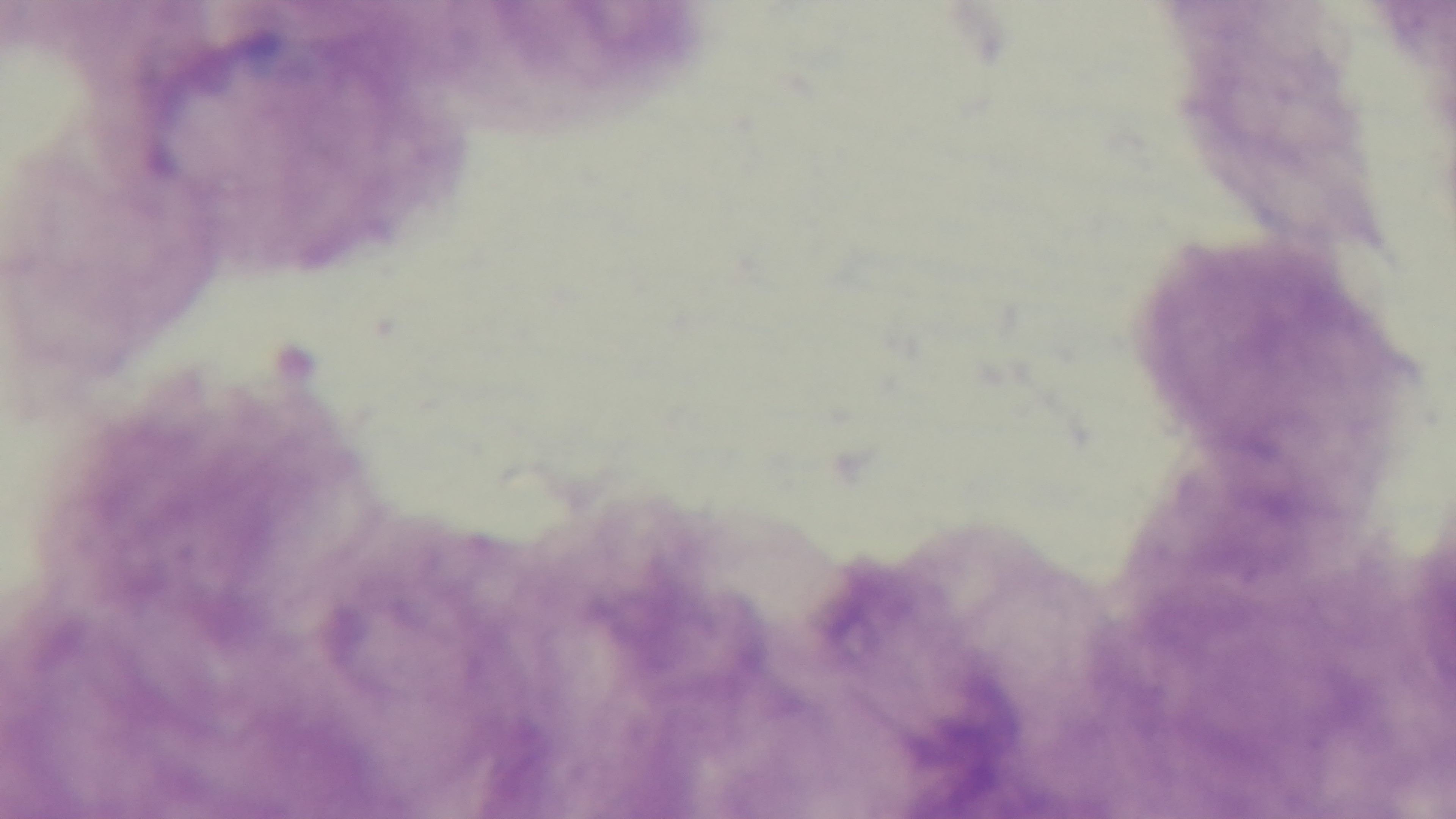 Captured with a mounted 4K digital camera. Giemsa stain. Malaria status: uninfected. Single field of view. Light microscopy. Preparation: thick blood film. Oil-immersion objective, 100x.